Identify the parasite.
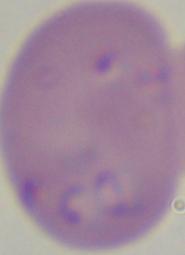
Babesia.

magnification = 1000x
modality = micrograph